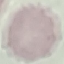 Malaria status: uninfected. Acquired by smartphone through the microscope eyepiece. Thin blood film. Giemsa stain. Cell patch, automatically extracted from a larger field of view and resized to 64 × 64 pixels.